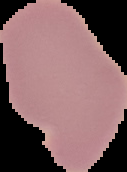

preparation = thin blood film
image type = cell region segmented out of the field of view; surrounding area masked to black
malaria status = uninfected
image size = 127×172 pixels